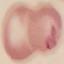

Malaria status: uninfected. Photographed with a smartphone camera at the microscope eyepiece. Cell patch, automatically extracted from a larger field of view and resized to 64 × 64 pixels. Giemsa-stained preparation. Thin smear of blood.